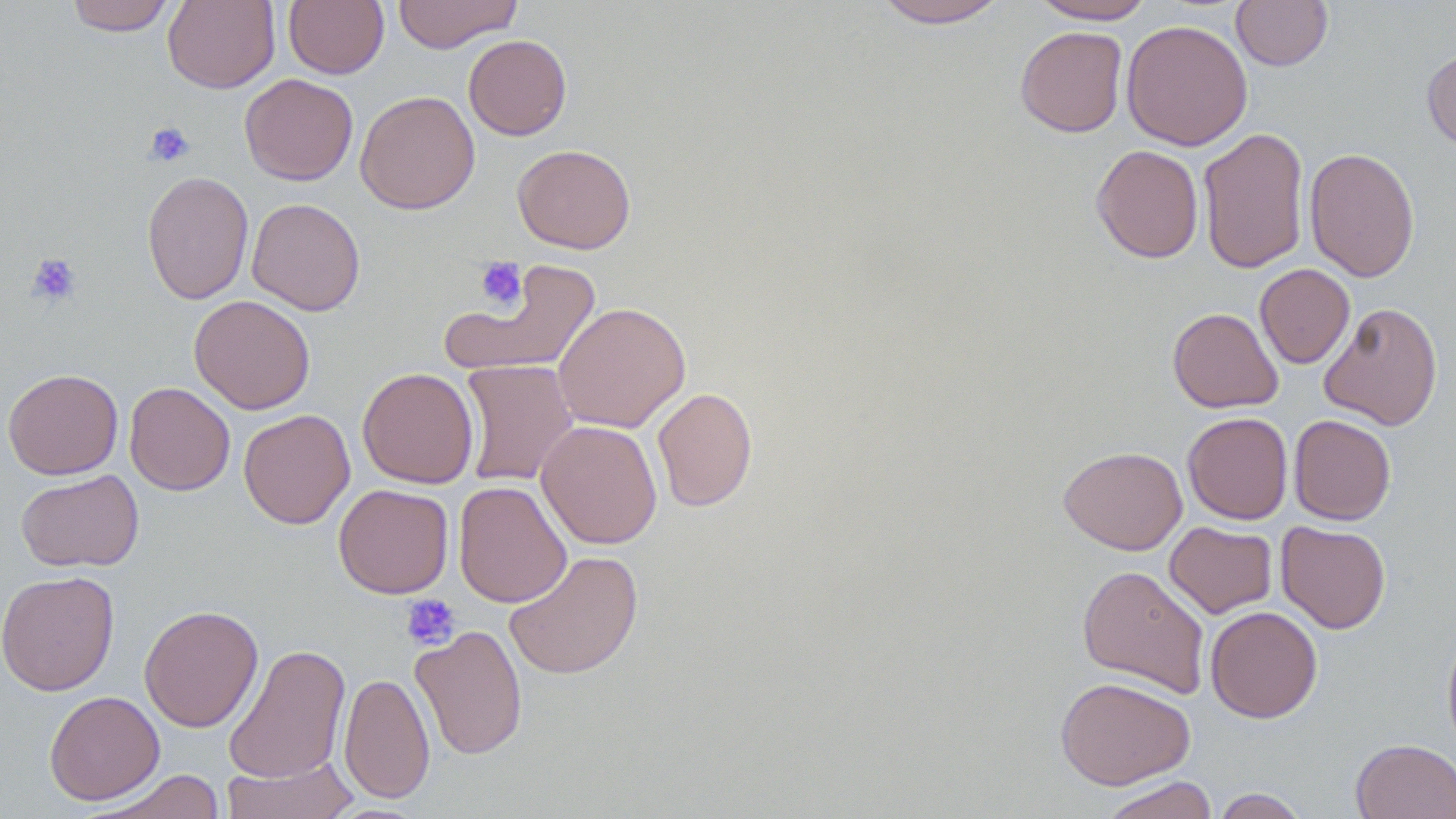
slide-level diagnosis = no evidence of blood parasites
magnification = 1000x
field of view = single
image size = 1456×819 pixels
modality = light microscopy
uninfected red blood cell locations = approximate bounding boxes as (x1,y1)-(x2,y2) corner pairs in pixels: (64,0)-(177,35), (163,0)-(280,93), (283,0)-(389,79), (392,0)-(522,53), (872,0)-(1009,28), (1030,0)-(1156,24), (1231,0)-(1333,71), (1121,19)-(1252,151), (1015,26)-(1128,137), (463,34)-(572,140), (1422,48)-(1456,153), (239,73)-(358,185), (355,91)-(480,214), (1197,126)-(1310,274), (512,144)-(636,254), (1091,144)-(1204,263), (1303,147)-(1420,282), (141,170)-(254,305), (246,197)-(365,315), (440,261)-(602,379), (1255,264)-(1355,368), (189,294)-(316,414), (553,301)-(690,433), (1318,301)-(1443,430), (1168,307)-(1283,413), (459,359)-(579,487), (357,367)-(479,488), (3,368)-(123,480), (124,381)-(235,496), (652,386)-(757,512), (239,409)-(355,529), (1182,412)-(1293,524), (1288,415)-(1396,525), (536,419)-(662,549), (1058,445)-(1187,555), (16,469)-(144,572), (453,480)-(572,608), (333,483)-(454,599), (1164,521)-(1278,618), (1276,521)-(1391,633), (504,550)-(643,680), (1077,565)-(1211,698), (1,570)-(120,696), (139,604)-(263,732), (1205,605)-(1323,723), (410,625)-(528,760), (1441,626)-(1456,757), (223,643)-(351,784), (338,672)-(435,803), (1054,676)-(1196,790), (43,690)-(165,805), (1351,738)-(1456,818), (221,754)-(359,819), (86,770)-(228,819), (1098,775)-(1220,819), (1210,788)-(1310,818)
platelet locations = approximate bounding boxes as (x1,y1)-(x2,y2) corner pairs in pixels: (144,121)-(194,167), (26,252)-(82,308), (474,256)-(527,312), (401,594)-(460,650)
stain = May-Grünwald-Giemsa
preparation = thin blood film